Name the parasite shown.
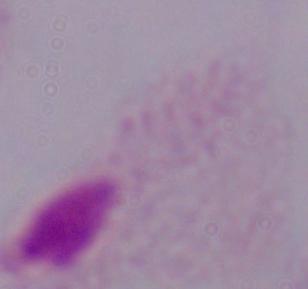
A trichomonad.

1000x magnification. Photomicrograph.